Assess the morphology of the red blood cells.
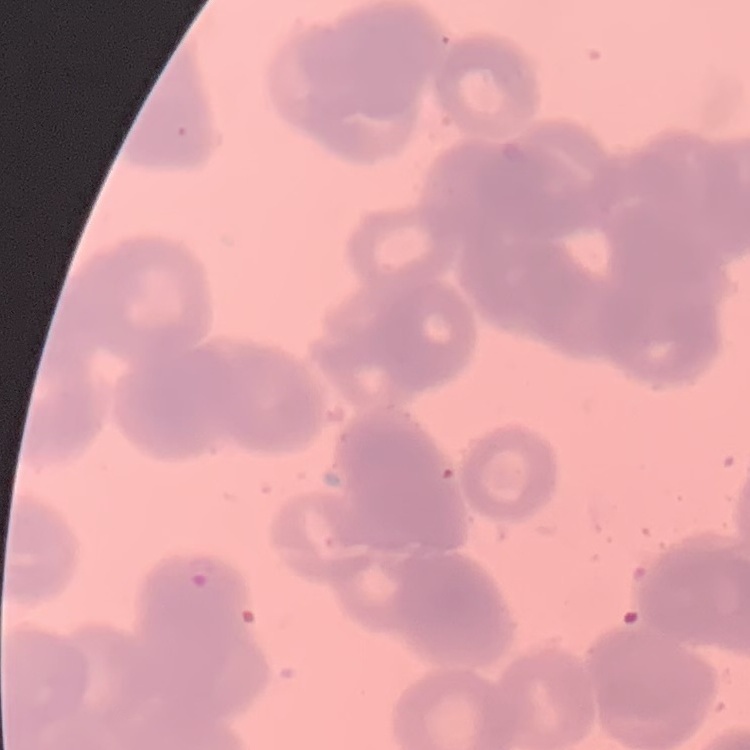
They show rouleaux formation.

preparation = thin peripheral smear
stain = Field's or Giemsa
image type = square crop of a larger photomicrograph